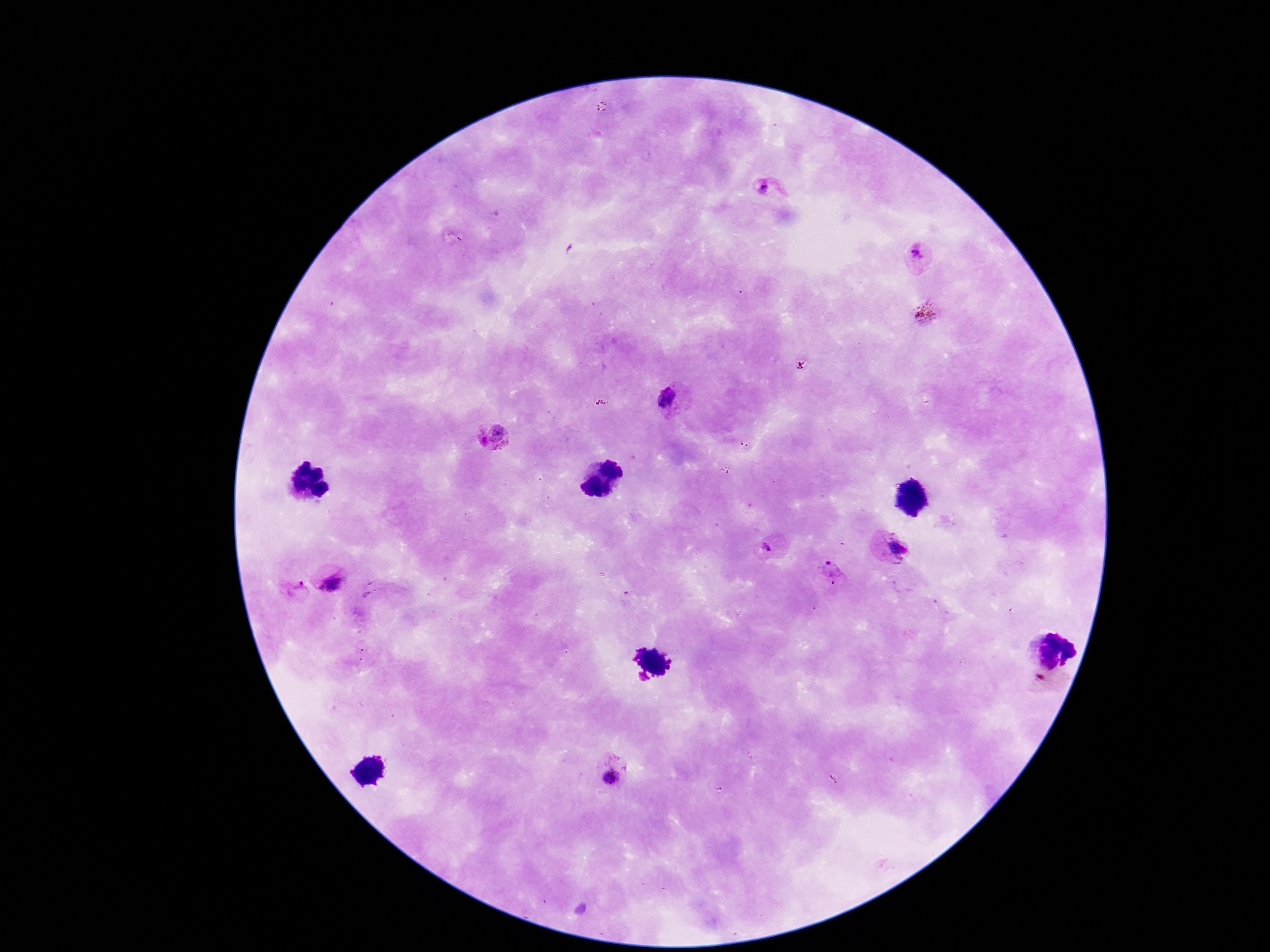
Approximate centers as (x, y) in pixels.
Summary:
  - Plasmodium parasite locations: (764, 187), (920, 253), (670, 395), (490, 434), (767, 547), (897, 549), (829, 568), (330, 580), (295, 590), (610, 776)
  - Preparation: thick blood film
  - Capture: smartphone camera through the microscope eyepiece
  - Patient malaria status: infected
  - Image size: 1270×952 pixels
  - Magnification: 100x
  - Stain: Giemsa
  - Field of view: single